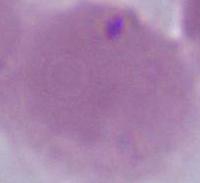

magnification = 1000x
modality = photomicrograph
identification = erythrocyte